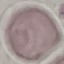
Summary:
  - Result: no malaria parasites seen
  - Capture: smartphone camera at the microscope eyepiece
  - Stain: Giemsa
  - Image type: cell patch, automatically extracted from a larger field of view and resized to 64 × 64 pixels
  - Preparation: thin blood smear